State which parasite is depicted.
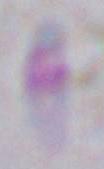
Toxoplasma gondii.

Summary:
  - Magnification: 1000x
  - Modality: micrograph